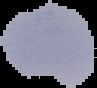

Summary:
  - Image size: 97×88 pixels
  - Preparation: thin blood film
  - Image type: cell region segmented out of the field of view; surrounding area masked to black
  - Malaria status: uninfected